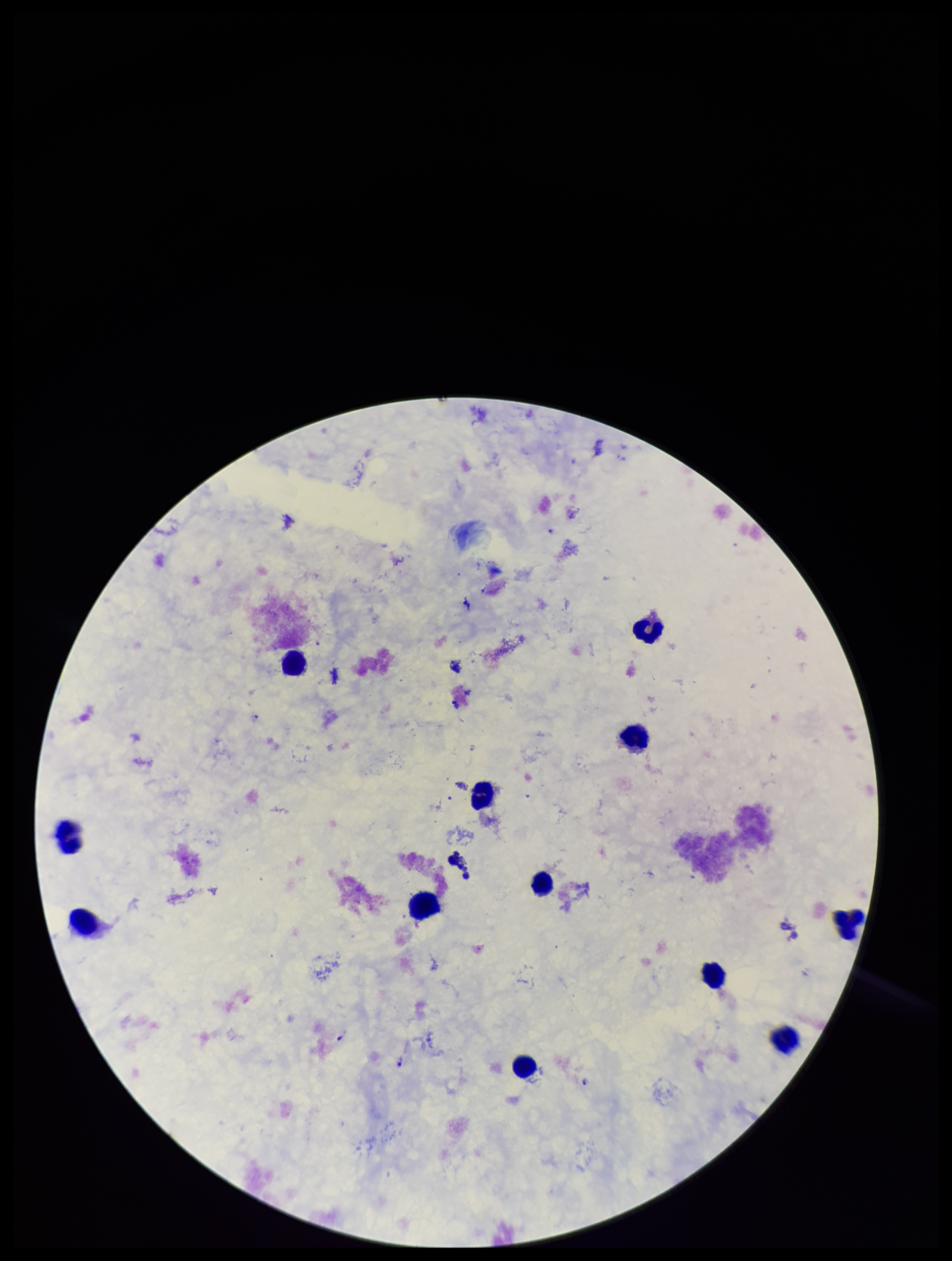
Plasmodium parasites = detected
image size = 952×1261 pixels
parasite count = 3
stain = Giemsa
species reported for this patient = Plasmodium falciparum
patient malaria status = infected
preparation = thick
field of view = one from this slide
capture = smartphone photograph through the microscope eyepiece
leukocyte count = 12